Describe the morphology of the red blood cells.
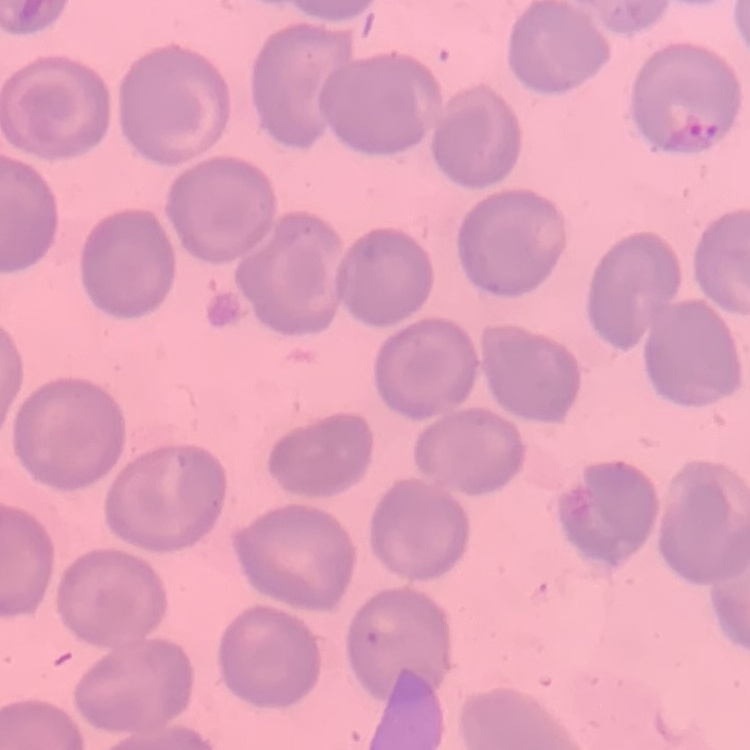
No rouleaux formation.

Square crop of a larger photomicrograph. Thin blood smear. Field's or Giemsa stain.